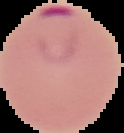
Summary:
  - Preparation: thin blood smear
  - Malaria status: parasitized
  - Image size: 124×133 pixels
  - Image type: cell region segmented out of the field of view; surrounding area masked to black